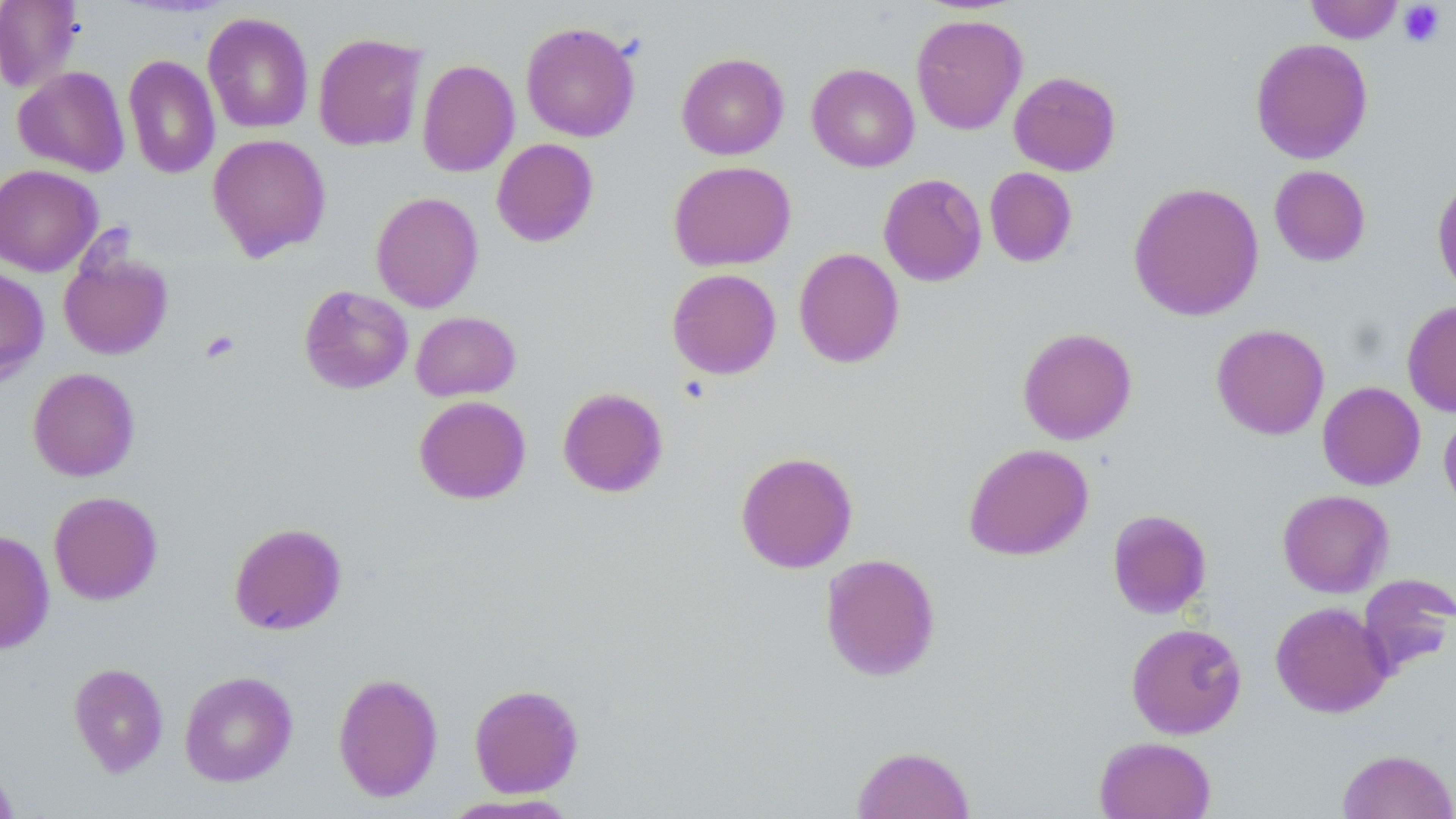
Summary:
  - Coordinate format: approximate bounding boxes as named x1/y1/x2/y2 corners in pixels
  - Platelet locations: (x1=1397, y1=1, x2=1446, y2=47), (x1=200, y1=330, x2=240, y2=364)
  - Uninfected red blood cell locations: (x1=0, y1=0, x2=84, y2=93), (x1=1305, y1=1, x2=1404, y2=43), (x1=202, y1=12, x2=314, y2=134), (x1=911, y1=14, x2=1028, y2=135), (x1=521, y1=21, x2=640, y2=142), (x1=313, y1=32, x2=428, y2=152), (x1=1250, y1=38, x2=1373, y2=164), (x1=676, y1=52, x2=789, y2=160), (x1=123, y1=54, x2=220, y2=179), (x1=417, y1=59, x2=519, y2=177), (x1=807, y1=63, x2=919, y2=172), (x1=12, y1=66, x2=130, y2=177), (x1=1008, y1=71, x2=1121, y2=176), (x1=207, y1=133, x2=331, y2=261), (x1=491, y1=138, x2=599, y2=247), (x1=668, y1=161, x2=796, y2=270), (x1=0, y1=164, x2=102, y2=277), (x1=1269, y1=165, x2=1371, y2=267), (x1=984, y1=167, x2=1078, y2=268), (x1=1432, y1=171, x2=1456, y2=299), (x1=878, y1=173, x2=987, y2=287), (x1=1128, y1=182, x2=1265, y2=321), (x1=371, y1=191, x2=483, y2=312), (x1=58, y1=244, x2=173, y2=361), (x1=793, y1=247, x2=905, y2=369), (x1=0, y1=267, x2=49, y2=385), (x1=666, y1=268, x2=782, y2=379), (x1=299, y1=285, x2=413, y2=395), (x1=1402, y1=299, x2=1456, y2=417), (x1=411, y1=311, x2=521, y2=401), (x1=1211, y1=323, x2=1330, y2=440), (x1=1017, y1=327, x2=1138, y2=445), (x1=27, y1=368, x2=140, y2=482), (x1=1317, y1=381, x2=1426, y2=490), (x1=557, y1=387, x2=669, y2=498), (x1=413, y1=395, x2=531, y2=505), (x1=1439, y1=407, x2=1456, y2=516), (x1=962, y1=443, x2=1093, y2=561), (x1=735, y1=451, x2=858, y2=573), (x1=1277, y1=489, x2=1393, y2=598), (x1=48, y1=491, x2=163, y2=605), (x1=1107, y1=509, x2=1212, y2=618), (x1=228, y1=522, x2=347, y2=635), (x1=0, y1=530, x2=54, y2=654), (x1=819, y1=553, x2=941, y2=681), (x1=1357, y1=574, x2=1456, y2=677), (x1=1270, y1=601, x2=1393, y2=718), (x1=1126, y1=622, x2=1248, y2=739), (x1=69, y1=662, x2=168, y2=777), (x1=179, y1=670, x2=298, y2=787), (x1=332, y1=672, x2=444, y2=802), (x1=468, y1=684, x2=584, y2=798), (x1=1093, y1=736, x2=1216, y2=819), (x1=851, y1=744, x2=976, y2=819), (x1=1337, y1=748, x2=1456, y2=819), (x1=0, y1=756, x2=19, y2=818), (x1=438, y1=794, x2=583, y2=818)
  - Slide-level diagnosis: no evidence of blood parasites
  - Preparation: thin blood smear
  - Image size: 1456×819 pixels
  - Stain: May-Grünwald-Giemsa
  - Field of view: one of a larger specimen
  - Magnification: 1000x
  - Modality: optical microscopy